Name the parasite shown.
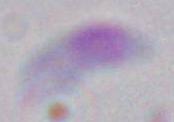

This is Toxoplasma gondii.

Summary:
  - Magnification: 1000x
  - Modality: photomicrograph